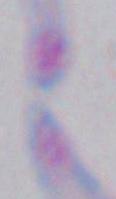
identification = Toxoplasma gondii
modality = photomicrograph
magnification = 1000x